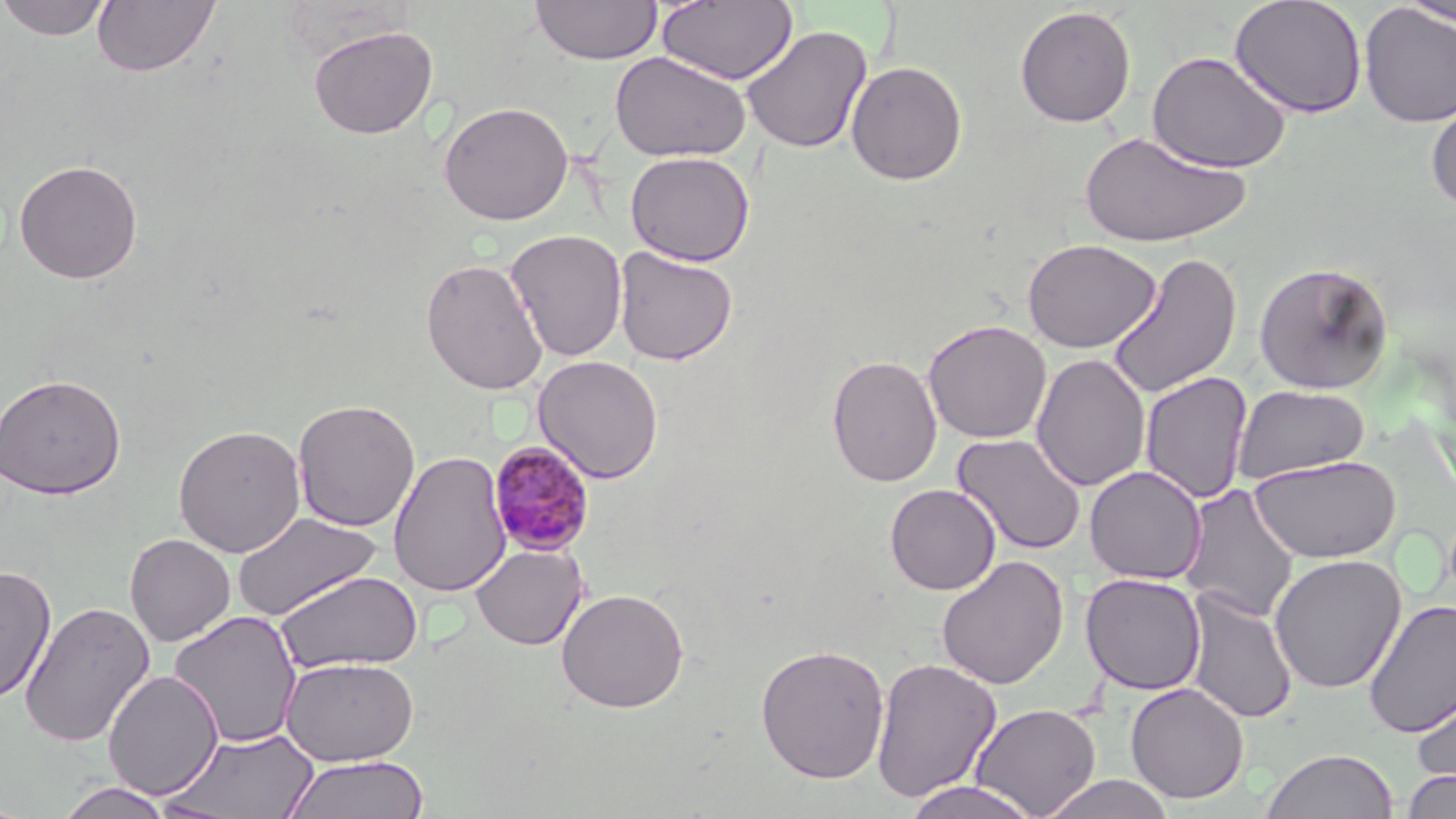
Summary:
  - Coordinate format: approximate bounding boxes as named x1/y1/x2/y2 corners in pixels
  - Uninfected red blood cell locations: (x1=0, y1=0, x2=112, y2=42), (x1=91, y1=0, x2=220, y2=78), (x1=531, y1=0, x2=662, y2=66), (x1=656, y1=0, x2=799, y2=85), (x1=1230, y1=0, x2=1368, y2=119), (x1=1396, y1=0, x2=1456, y2=30), (x1=1358, y1=4, x2=1456, y2=128), (x1=1014, y1=5, x2=1137, y2=128), (x1=308, y1=24, x2=438, y2=139), (x1=741, y1=25, x2=873, y2=155), (x1=1146, y1=50, x2=1291, y2=174), (x1=609, y1=52, x2=751, y2=162), (x1=846, y1=60, x2=968, y2=185), (x1=1426, y1=96, x2=1456, y2=213), (x1=438, y1=101, x2=574, y2=225), (x1=1079, y1=128, x2=1250, y2=248), (x1=625, y1=151, x2=755, y2=266), (x1=14, y1=158, x2=143, y2=284), (x1=504, y1=229, x2=628, y2=362), (x1=1021, y1=239, x2=1161, y2=353), (x1=613, y1=246, x2=739, y2=366), (x1=1106, y1=251, x2=1242, y2=400), (x1=420, y1=258, x2=548, y2=396), (x1=1253, y1=261, x2=1395, y2=395), (x1=923, y1=319, x2=1052, y2=444), (x1=1031, y1=353, x2=1151, y2=493), (x1=826, y1=354, x2=942, y2=487), (x1=533, y1=355, x2=664, y2=484), (x1=1140, y1=371, x2=1253, y2=505), (x1=0, y1=373, x2=126, y2=499), (x1=1233, y1=384, x2=1371, y2=484), (x1=292, y1=398, x2=420, y2=532), (x1=172, y1=424, x2=306, y2=558), (x1=951, y1=433, x2=1088, y2=557), (x1=388, y1=449, x2=512, y2=598), (x1=1248, y1=455, x2=1401, y2=563), (x1=1084, y1=465, x2=1206, y2=585), (x1=1178, y1=483, x2=1301, y2=623), (x1=884, y1=484, x2=1001, y2=595), (x1=232, y1=511, x2=381, y2=621), (x1=125, y1=533, x2=235, y2=646), (x1=471, y1=544, x2=588, y2=650), (x1=1269, y1=553, x2=1407, y2=694), (x1=936, y1=555, x2=1069, y2=690), (x1=0, y1=563, x2=57, y2=703), (x1=276, y1=569, x2=423, y2=674), (x1=1080, y1=572, x2=1207, y2=695), (x1=555, y1=588, x2=689, y2=713), (x1=1184, y1=588, x2=1299, y2=726), (x1=1363, y1=598, x2=1456, y2=739), (x1=19, y1=600, x2=155, y2=748), (x1=168, y1=611, x2=303, y2=749), (x1=755, y1=644, x2=891, y2=783), (x1=280, y1=656, x2=419, y2=767), (x1=870, y1=656, x2=1002, y2=804), (x1=103, y1=670, x2=223, y2=799), (x1=1411, y1=677, x2=1456, y2=793), (x1=1125, y1=681, x2=1249, y2=804), (x1=970, y1=703, x2=1102, y2=817), (x1=164, y1=727, x2=320, y2=818), (x1=1261, y1=748, x2=1398, y2=819), (x1=281, y1=754, x2=431, y2=819), (x1=1401, y1=769, x2=1456, y2=819), (x1=1038, y1=774, x2=1177, y2=819), (x1=901, y1=779, x2=1043, y2=818), (x1=55, y1=781, x2=175, y2=818)
  - Plasmodium malariae-infected red blood cell locations: (x1=486, y1=440, x2=597, y2=556)
  - Slide-level diagnosis: Plasmodium malariae
  - Stain: May-Grünwald-Giemsa
  - Preparation: thin blood film
  - Modality: light microscopy
  - Magnification: 1000x
  - Image size: 1456×819 pixels
  - Field of view: single